Assess for malaria.
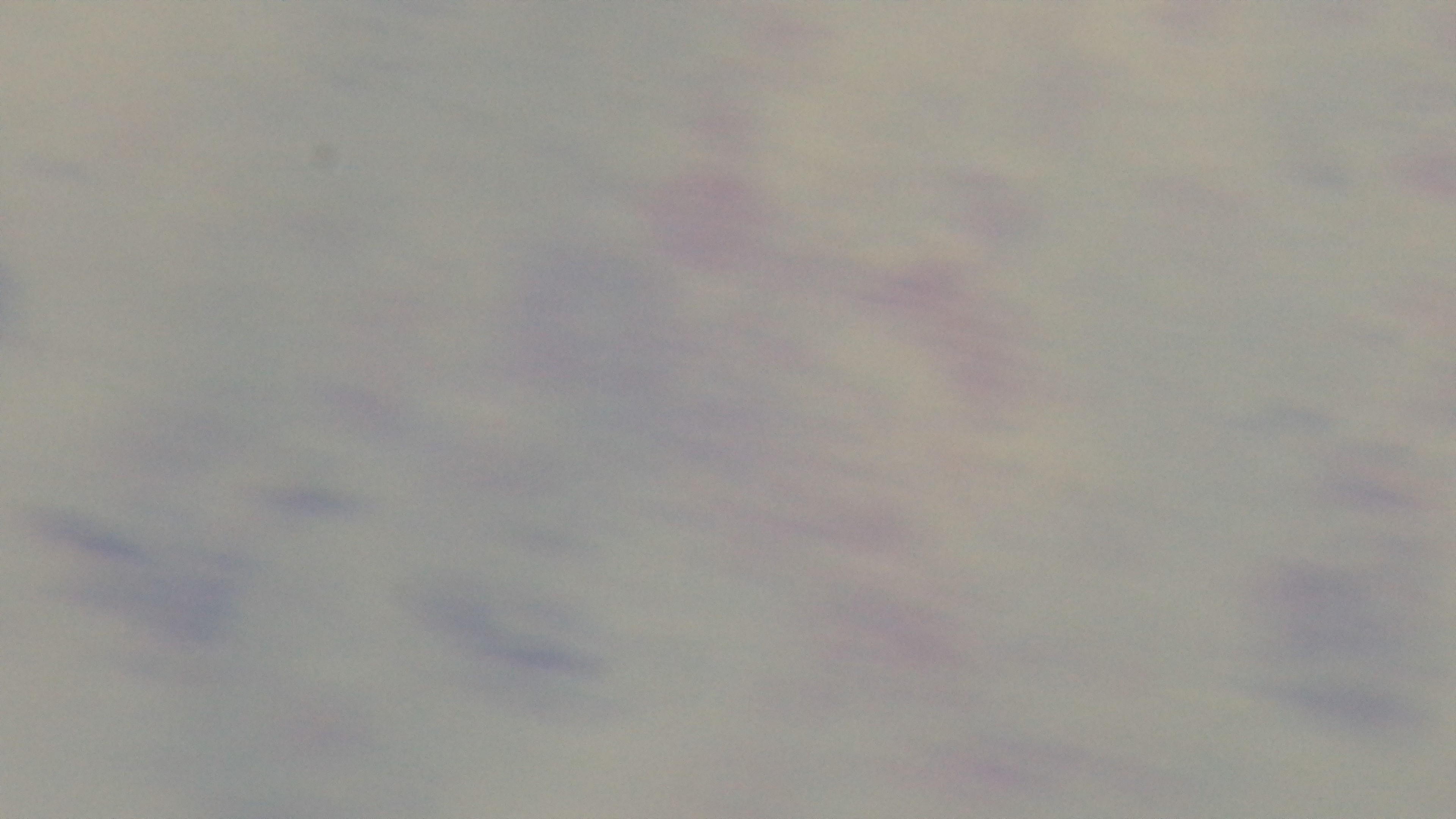
Negative.

objective = 100x oil immersion
stain = Giemsa
capture = mounted 4K digital camera
modality = light microscopy
preparation = thick blood film
field of view = one from the slide